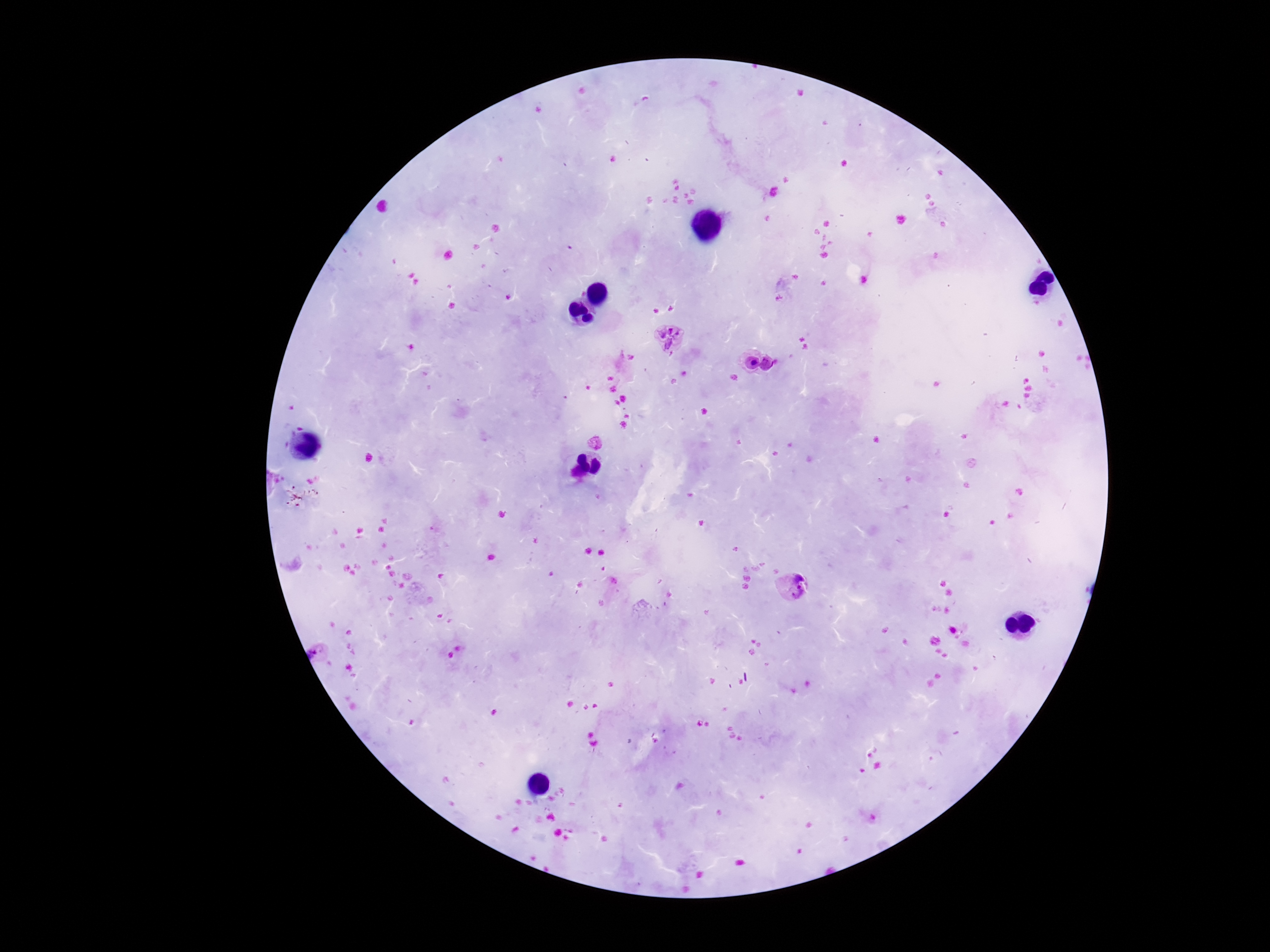 Approximate centers as (x, y) in pixels. Plasmodium parasite locations: (668, 337), (793, 588). One field from this slide. Smartphone photograph taken through the microscope eyepiece. Thick blood smear. Image is 1270×952 pixels. 100x magnification. Giemsa stain. Patient malaria status: infected.